Name the blood parasite species.
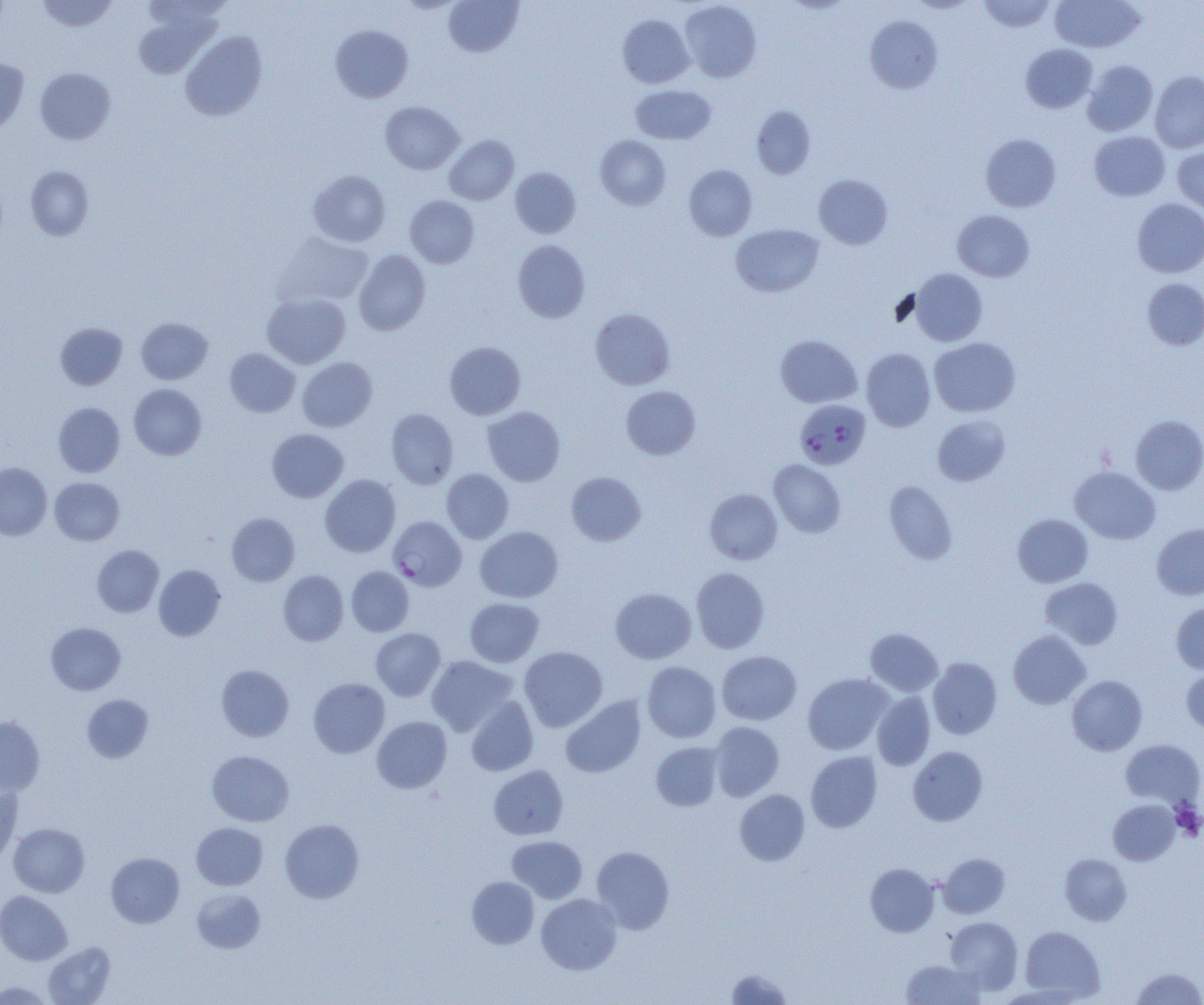

Plasmodium falciparum.

Approximate bounding boxes as [x1, y1, x2, y2] in pixels. Uninfected red blood cell locations: [36, 0, 118, 32], [141, 0, 230, 30], [444, 0, 523, 57], [977, 0, 1056, 32], [1050, 0, 1145, 53], [680, 1, 762, 83], [133, 9, 223, 79], [618, 14, 694, 88], [865, 16, 943, 93], [330, 24, 413, 103], [181, 31, 267, 121], [1020, 44, 1097, 113], [0, 58, 29, 135], [1083, 60, 1158, 136], [35, 67, 115, 144], [1150, 71, 1204, 153], [631, 84, 716, 144], [380, 101, 464, 174], [751, 105, 816, 179], [1089, 131, 1170, 201], [980, 134, 1061, 212], [444, 135, 519, 205], [595, 135, 671, 209], [1173, 147, 1204, 214], [684, 165, 757, 241], [25, 167, 93, 240], [510, 167, 581, 238], [308, 169, 391, 247], [814, 173, 893, 249], [405, 196, 479, 268], [1133, 198, 1204, 278], [953, 210, 1034, 282], [731, 224, 824, 297], [274, 232, 373, 307], [513, 240, 590, 322], [354, 250, 431, 335], [909, 268, 988, 346], [1142, 278, 1204, 350], [261, 293, 350, 368], [590, 308, 676, 390], [136, 317, 213, 384], [55, 322, 127, 390], [775, 334, 861, 408], [929, 337, 1020, 417], [444, 341, 525, 420], [225, 348, 300, 417], [861, 348, 935, 432], [297, 357, 377, 432], [129, 384, 206, 460], [621, 386, 700, 460], [53, 402, 125, 477], [482, 406, 565, 486], [386, 408, 458, 489], [932, 414, 1011, 486], [1131, 415, 1204, 494], [266, 429, 348, 502], [769, 459, 846, 537], [0, 463, 52, 540], [1069, 466, 1161, 544], [442, 468, 514, 543], [566, 472, 646, 546], [320, 474, 400, 557], [50, 477, 124, 546], [884, 480, 958, 564], [705, 489, 782, 564], [227, 513, 300, 586], [1013, 514, 1093, 587], [1151, 523, 1204, 600], [475, 526, 563, 603], [92, 545, 164, 617], [153, 564, 226, 641], [346, 566, 414, 636], [691, 567, 770, 653], [278, 570, 348, 645], [1040, 578, 1123, 649], [610, 588, 696, 664], [464, 597, 544, 667], [1171, 602, 1204, 673], [46, 622, 125, 695], [371, 628, 445, 700], [865, 628, 943, 696], [1008, 630, 1091, 709], [519, 646, 607, 731], [717, 651, 801, 725], [426, 656, 516, 735], [928, 657, 1002, 739], [642, 662, 721, 742], [216, 664, 294, 742], [1181, 667, 1204, 734], [802, 673, 893, 755], [1067, 675, 1147, 755], [308, 678, 390, 758], [872, 692, 935, 770], [83, 695, 153, 762], [466, 695, 538, 776], [560, 695, 646, 778], [0, 716, 44, 794], [372, 716, 452, 794], [709, 721, 784, 801], [1120, 739, 1204, 809], [651, 742, 724, 811], [908, 746, 988, 826], [207, 750, 294, 826], [806, 751, 883, 832], [489, 765, 568, 840], [0, 783, 22, 866], [734, 789, 810, 866], [1108, 799, 1180, 865], [280, 818, 364, 903], [8, 822, 89, 897], [191, 822, 268, 890], [507, 835, 587, 903], [591, 846, 674, 933], [106, 852, 184, 928], [938, 853, 1010, 919], [1060, 854, 1132, 925], [865, 863, 939, 937], [467, 876, 539, 949], [191, 888, 266, 953], [0, 891, 72, 965], [536, 893, 622, 974], [945, 916, 1023, 993], [1020, 926, 1105, 1001], [42, 942, 115, 1005], [901, 958, 985, 1004], [1130, 966, 1204, 1005], [725, 968, 794, 1004], [1, 980, 56, 1004]. Plasmodium falciparum-infected red blood cell locations: [795, 399, 871, 470], [388, 516, 466, 590]. Platelet locations: [1171, 802, 1204, 840]. One field of a larger specimen. Light microscopy. Image is 1204×1005 pixels. Thin blood film. 1000x magnification.